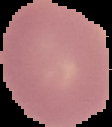
Image is 112×127 pixels. From a thin blood film. Malaria status: uninfected. Cell region segmented out of the field of view; the surrounding area is masked to black.